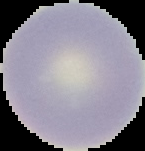

{
  "image_type": "segmented cell region with the area outside set to black",
  "preparation": "thin blood film",
  "image_size": "145×151 pixels",
  "malaria_status": "uninfected"
}